Identify the cell.
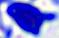
This is a leukocyte.

modality: photomicrograph
magnification: 400x